Identify the blood parasite species.
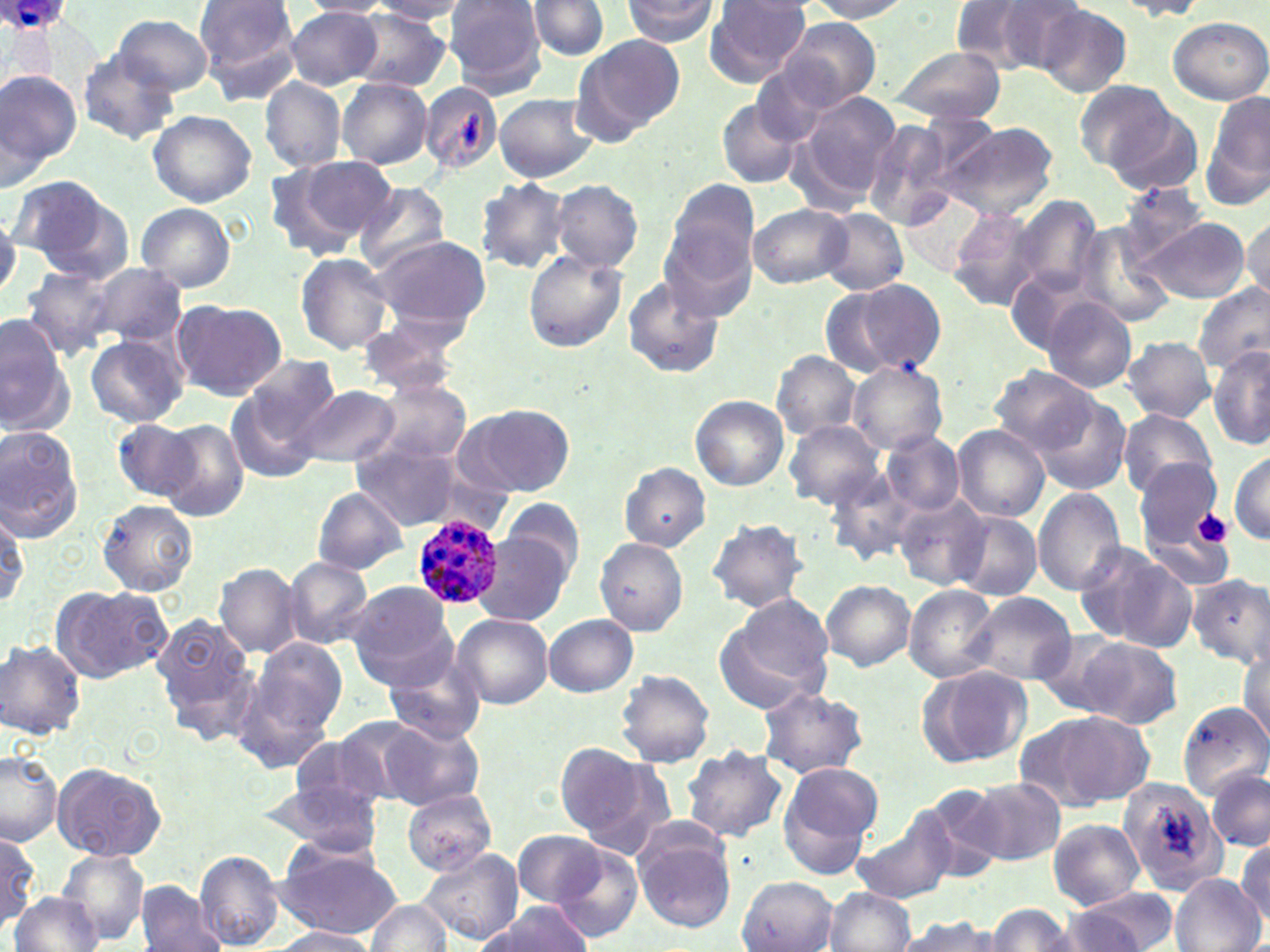

Plasmodium ovale.

Approximate bounding boxes as (x1, y1, x2, y2) in pixels. Uninfected red blood cell locations: (193, 0, 299, 100), (622, 0, 719, 44), (803, 0, 913, 21), (961, 0, 1086, 76), (297, 1, 395, 17), (369, 1, 476, 22), (444, 1, 546, 93), (527, 1, 609, 59), (1114, 1, 1212, 19), (704, 2, 814, 87), (1034, 5, 1131, 97), (284, 8, 384, 89), (347, 9, 453, 91), (112, 13, 212, 95), (775, 15, 884, 112), (1167, 16, 1269, 105), (570, 34, 687, 142), (889, 44, 1006, 124), (77, 51, 179, 145), (0, 68, 81, 178), (259, 77, 347, 173), (337, 78, 433, 169), (1075, 80, 1175, 171), (419, 83, 503, 174), (792, 90, 900, 206), (1203, 90, 1270, 209), (493, 93, 598, 183), (717, 98, 805, 188), (1107, 109, 1202, 195), (149, 110, 257, 207), (861, 116, 969, 235), (940, 122, 1059, 221), (269, 154, 396, 257), (8, 178, 123, 272), (477, 178, 571, 274), (549, 180, 644, 273), (662, 180, 760, 309), (355, 182, 449, 274), (1115, 184, 1214, 265), (901, 189, 992, 279), (1008, 194, 1103, 302), (135, 202, 237, 292), (748, 202, 853, 290), (947, 207, 1044, 311), (819, 208, 909, 296), (1244, 217, 1270, 304), (1138, 218, 1250, 304), (1073, 224, 1175, 328), (369, 235, 490, 332), (523, 252, 627, 352), (295, 253, 394, 353), (90, 263, 187, 349), (1008, 264, 1100, 355), (20, 265, 123, 360), (622, 277, 722, 378), (820, 279, 944, 378), (1195, 283, 1270, 375), (1039, 297, 1137, 394), (171, 300, 287, 400), (355, 314, 463, 396), (0, 315, 74, 437), (85, 334, 187, 427), (1122, 336, 1214, 422), (1208, 345, 1269, 451), (772, 350, 861, 439), (238, 354, 343, 453), (847, 362, 947, 453), (989, 368, 1098, 456), (367, 378, 472, 467), (225, 382, 329, 483), (292, 383, 400, 468), (690, 394, 789, 491), (1033, 394, 1133, 497), (460, 404, 575, 498), (1117, 409, 1219, 498), (112, 418, 202, 503), (159, 419, 249, 521), (784, 419, 885, 510), (0, 425, 84, 541), (953, 426, 1050, 521), (882, 431, 964, 515), (353, 442, 466, 530), (1229, 448, 1270, 545), (1135, 458, 1232, 572), (621, 463, 710, 551), (824, 466, 920, 568), (311, 487, 407, 574), (1032, 487, 1127, 595), (893, 494, 991, 590), (505, 497, 586, 576), (96, 499, 198, 596), (0, 503, 30, 611), (948, 510, 1042, 601), (707, 516, 810, 613), (475, 532, 572, 624), (594, 537, 688, 636), (1072, 540, 1192, 650), (282, 557, 373, 650), (215, 564, 302, 656), (1187, 573, 1270, 667), (821, 580, 916, 672), (346, 582, 456, 688), (903, 584, 999, 683), (51, 586, 172, 683), (963, 592, 1078, 688), (716, 597, 834, 713), (153, 613, 255, 734), (452, 613, 552, 709), (544, 615, 638, 697), (1070, 634, 1183, 728), (247, 637, 348, 744), (1, 638, 86, 738), (1238, 642, 1270, 746), (385, 653, 486, 746), (915, 666, 1032, 768), (616, 669, 715, 769), (757, 686, 869, 778), (1177, 701, 1269, 799), (1021, 710, 1156, 811), (331, 717, 438, 804), (381, 720, 485, 810), (554, 744, 658, 843), (683, 746, 788, 844), (0, 749, 63, 847), (779, 759, 884, 866), (51, 762, 166, 862), (1206, 766, 1269, 854), (260, 778, 385, 856), (967, 778, 1065, 866), (1119, 779, 1228, 897), (914, 784, 1011, 881), (401, 789, 499, 876), (852, 817, 955, 904), (1050, 819, 1144, 908), (634, 823, 736, 931), (0, 828, 42, 930), (512, 829, 607, 906), (1234, 833, 1269, 927), (274, 838, 401, 939), (552, 846, 643, 942), (415, 848, 525, 946), (57, 849, 150, 947), (196, 849, 284, 950), (1172, 874, 1263, 952), (737, 878, 836, 950), (136, 882, 225, 952), (1067, 886, 1183, 951), (823, 887, 914, 952), (10, 892, 101, 951), (369, 897, 450, 951), (479, 903, 594, 951), (984, 904, 1081, 952), (895, 915, 1000, 952), (273, 927, 376, 952). Platelet locations: (455, 109, 483, 154), (1192, 509, 1232, 548). Plasmodium ovale-infected red blood cell locations: (0, 0, 75, 37), (411, 514, 507, 608). One field of a larger specimen. May-Grünwald-Giemsa-stained preparation. 1000x magnification. Thin blood film. Image is 1270×952 pixels. Optical microscopy.